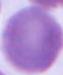
A red blood cell is seen. 1000x magnification. Photomicrograph.